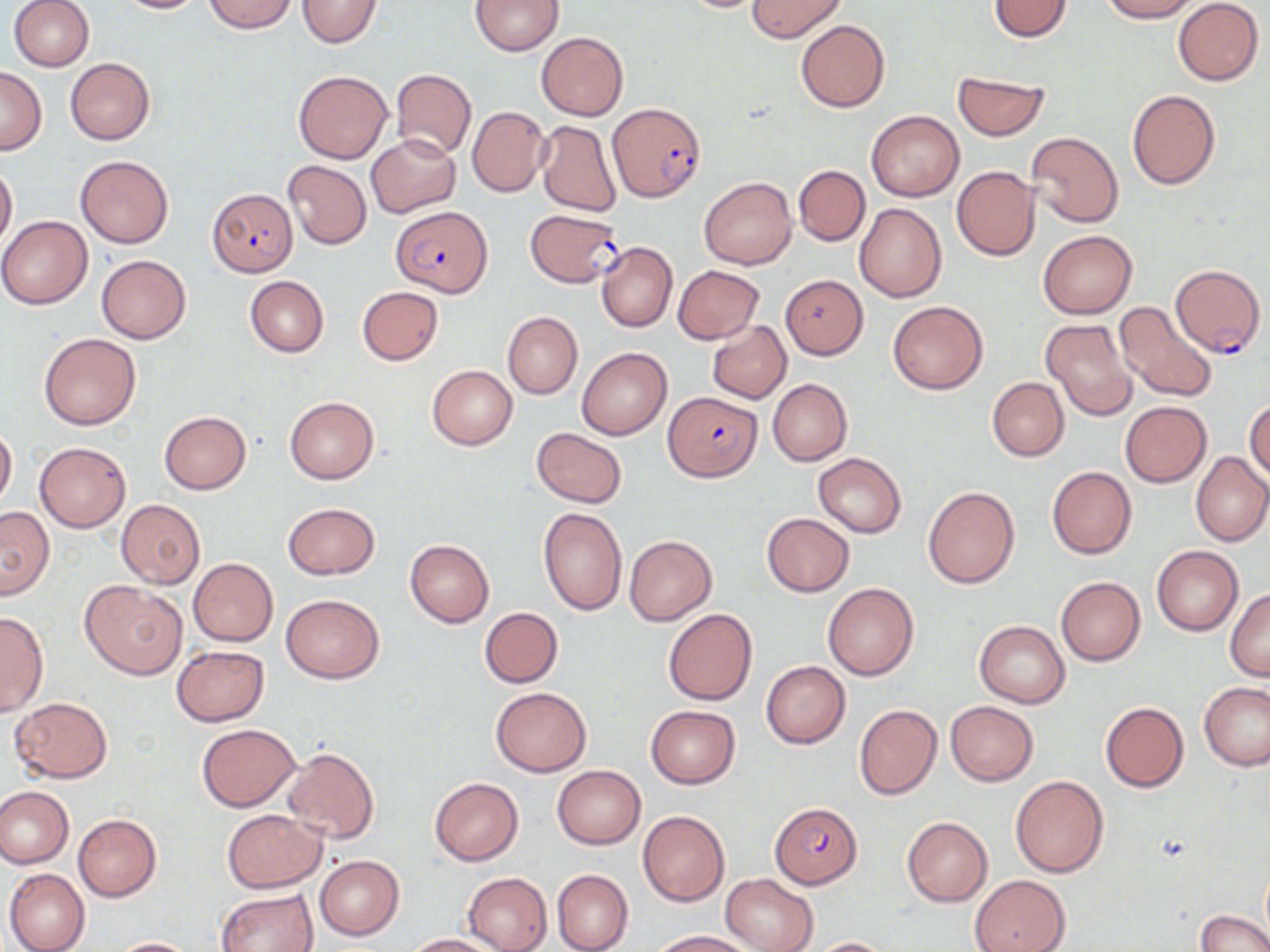

{
  "slide_level_diagnosis": "Plasmodium falciparum",
  "magnification": "1000x",
  "image_size": "1270×952 pixels",
  "field_of_view": "single",
  "plasmodium_falciparum_infected_red_blood_cell_locations": "approximate bounding boxes as [x1, y1, x2, y2] in pixels: [608, 103, 706, 201], [206, 188, 299, 277], [390, 206, 494, 296], [524, 209, 624, 289], [1168, 261, 1264, 358], [666, 390, 761, 482], [770, 801, 861, 887]",
  "preparation": "thin blood smear",
  "stain": "May-Grünwald-Giemsa",
  "uninfected_red_blood_cell_locations": "approximate bounding boxes as [x1, y1, x2, y2] in pixels: [10, 0, 94, 72], [113, 0, 209, 14], [203, 0, 297, 33], [296, 0, 382, 47], [748, 0, 845, 41], [987, 0, 1074, 43], [1099, 0, 1199, 22], [472, 1, 563, 55], [673, 1, 774, 13], [1173, 1, 1264, 85], [796, 20, 889, 111], [536, 32, 628, 120], [65, 57, 155, 144], [0, 66, 47, 154], [391, 67, 475, 160], [293, 69, 393, 163], [952, 71, 1050, 140], [1127, 89, 1221, 189], [467, 105, 549, 198], [866, 110, 964, 201], [535, 120, 621, 218], [1026, 131, 1124, 228], [367, 135, 460, 217], [75, 155, 173, 248], [283, 160, 371, 249], [0, 162, 17, 249], [794, 165, 870, 246], [952, 165, 1041, 261], [699, 177, 797, 268], [854, 203, 946, 302], [0, 215, 94, 309], [1038, 230, 1136, 318], [597, 242, 677, 332], [97, 255, 191, 343], [672, 266, 763, 343], [245, 275, 328, 356], [779, 275, 867, 358], [356, 286, 444, 365], [887, 301, 988, 394], [1114, 302, 1218, 403], [503, 311, 582, 399], [1041, 318, 1138, 421], [707, 320, 791, 403], [40, 333, 141, 430], [577, 346, 672, 440], [427, 365, 517, 450], [987, 376, 1069, 461], [767, 379, 852, 466], [285, 397, 379, 483], [1246, 398, 1270, 485], [1119, 401, 1211, 487], [159, 411, 251, 494], [0, 426, 16, 508], [531, 427, 628, 507], [35, 442, 131, 532], [1191, 452, 1270, 547], [814, 453, 906, 537], [1047, 466, 1136, 559], [923, 486, 1020, 588], [117, 499, 204, 588], [283, 502, 379, 579], [0, 506, 54, 598], [538, 507, 626, 616], [762, 512, 854, 596], [624, 535, 716, 626], [405, 539, 494, 627], [1152, 545, 1243, 636], [188, 559, 278, 646], [1055, 576, 1145, 666], [80, 581, 186, 679], [822, 583, 919, 680], [1225, 588, 1270, 681], [282, 593, 383, 683], [479, 607, 564, 688], [662, 608, 757, 705], [0, 609, 48, 717], [974, 620, 1069, 707], [172, 645, 268, 726], [761, 661, 850, 749], [1200, 683, 1270, 770], [491, 687, 591, 776], [9, 698, 113, 783], [945, 701, 1038, 786], [1100, 701, 1188, 792], [854, 703, 942, 800], [645, 706, 742, 789], [196, 722, 301, 812], [282, 746, 379, 843], [552, 765, 645, 848], [1009, 775, 1109, 878], [430, 778, 523, 865], [0, 787, 73, 869], [221, 809, 327, 892], [638, 810, 729, 906], [73, 814, 161, 901], [901, 817, 993, 906], [314, 855, 405, 940], [4, 867, 91, 952], [552, 869, 633, 952], [463, 872, 553, 952], [722, 873, 819, 952], [970, 874, 1072, 952], [217, 888, 319, 952], [1194, 909, 1269, 952], [652, 930, 754, 951], [405, 933, 502, 951], [805, 936, 897, 952], [110, 937, 199, 952]",
  "modality": "optical microscopy"
}